Assess the morphology of the red blood cells.
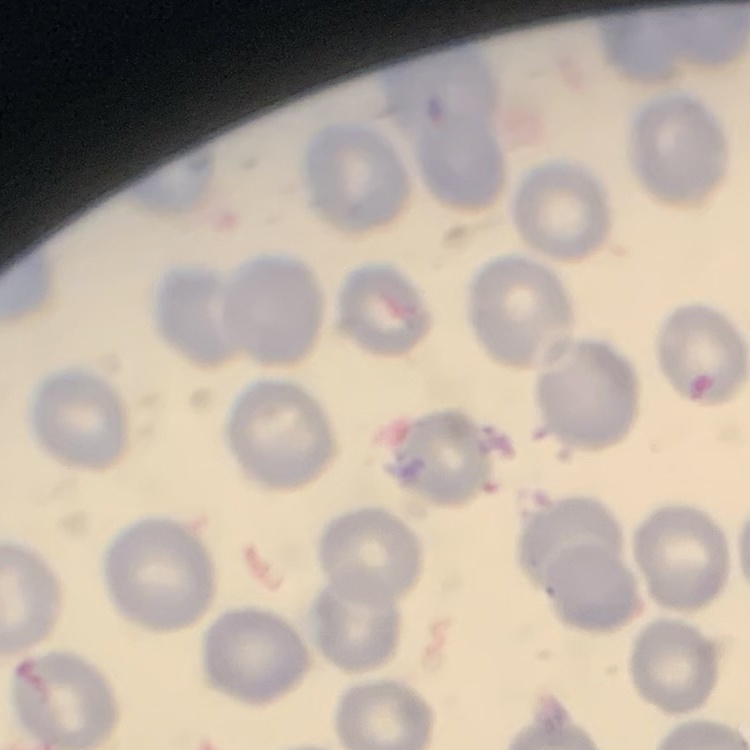
No rouleaux formation.

Thin blood film. One tile cut from a larger photomicrograph. Field's or Giemsa stain.